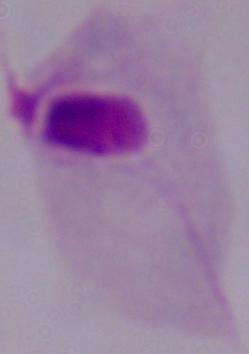

A trichomonad is shown. Photomicrograph. Captured at 1000x magnification.